Name the parasite shown.
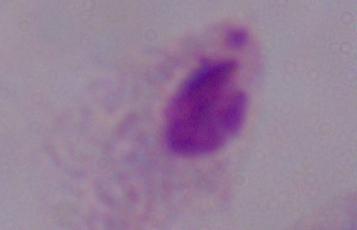

A trichomonad.

Summary:
  - Magnification: 1000x
  - Modality: micrograph